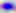 Toxoplasma gondii is seen. Micrograph. 400x magnification.